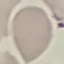

Malaria status: uninfected. Automatically extracted cell patch, resized to 64 × 64 pixels. Thin smear of blood. Acquired by smartphone through the microscope eyepiece. Giemsa stain.